Outline each Plasmodium falciparum-infected red blood cell.
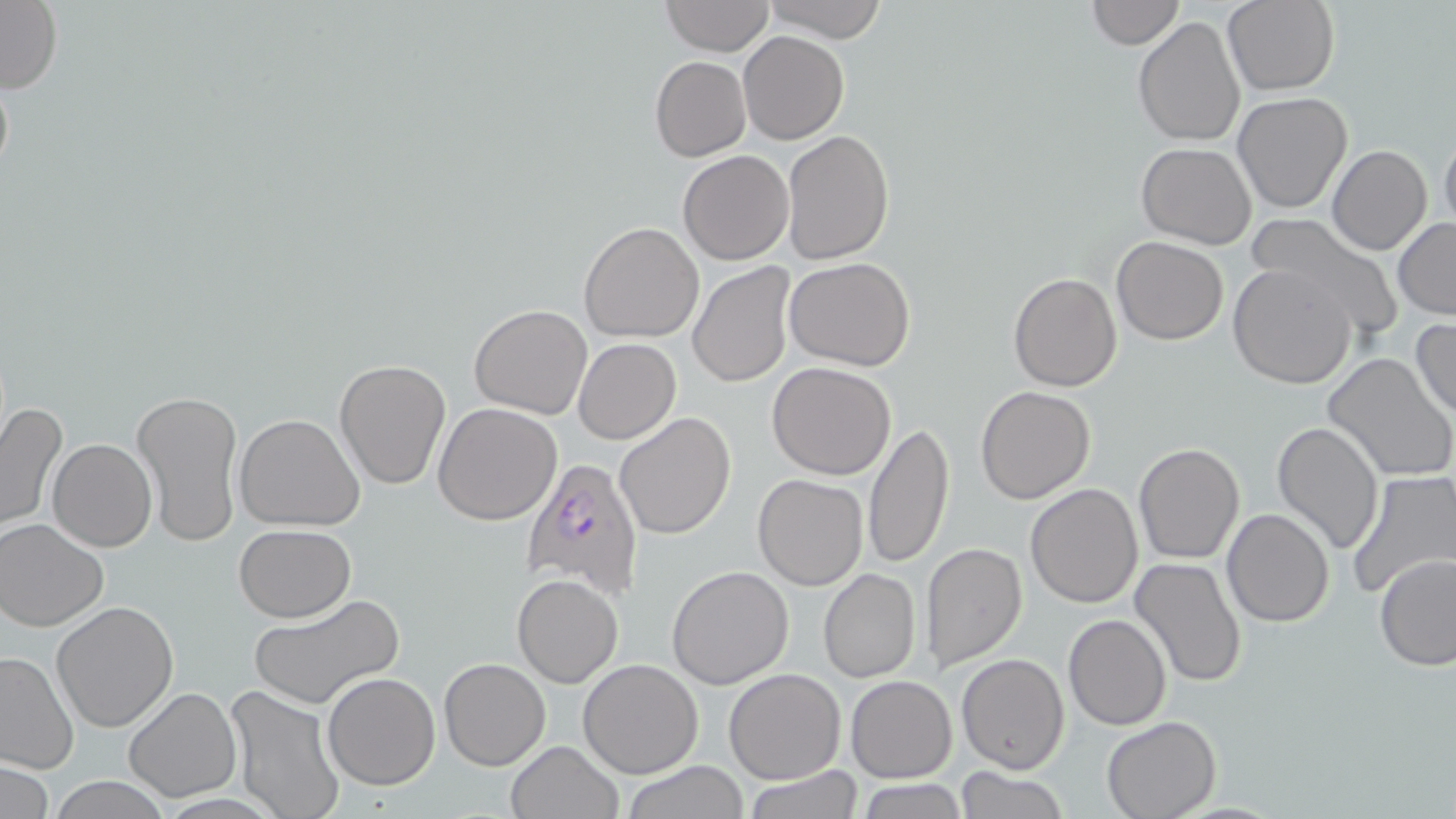

Approximate bounding boxes as (x1,y1)-(x2,y2) corner pairs in pixels.
Plasmodium falciparum-infected red blood cells: (520,457)-(645,599).

Uninfected red blood cell locations: (759,0)-(889,43), (660,1)-(775,56), (1084,1)-(1183,49), (1222,1)-(1341,96), (0,2)-(61,95), (1133,16)-(1247,148), (738,29)-(850,145), (650,55)-(751,161), (1232,93)-(1352,213), (1439,124)-(1456,231), (782,128)-(894,266), (1136,142)-(1257,248), (1327,144)-(1432,256), (678,149)-(794,264), (1242,213)-(1404,341), (1393,218)-(1456,320), (578,221)-(704,343), (1111,236)-(1229,346), (785,257)-(916,370), (688,262)-(795,388), (1228,264)-(1356,388), (1008,272)-(1123,391), (469,304)-(594,419), (1410,318)-(1456,420), (573,338)-(681,444), (1322,352)-(1455,483), (335,358)-(450,490), (766,362)-(898,480), (975,386)-(1095,503), (133,388)-(244,549), (1,399)-(69,534), (433,402)-(563,525), (614,411)-(737,540), (233,413)-(365,531), (863,420)-(954,570), (1269,420)-(1382,556), (47,439)-(157,552), (1132,443)-(1245,565), (1346,471)-(1456,601), (752,474)-(868,590), (1026,482)-(1143,607), (1222,508)-(1335,627), (0,519)-(109,632), (233,524)-(357,621), (918,542)-(1030,673), (1375,554)-(1456,670), (1128,556)-(1248,689), (666,565)-(794,690), (818,568)-(921,683), (512,574)-(623,686), (248,592)-(405,710), (50,602)-(179,733), (1062,612)-(1172,730), (0,652)-(77,774), (956,653)-(1069,772), (438,658)-(551,771), (577,658)-(704,778), (724,668)-(847,784), (321,673)-(441,791), (845,675)-(958,783), (223,684)-(347,819), (122,687)-(241,802), (1100,716)-(1220,819), (506,740)-(623,819), (2,760)-(53,819), (619,761)-(751,818), (952,765)-(1070,819), (746,766)-(865,819), (46,777)-(175,817), (858,779)-(968,818). Slide-level diagnosis: Plasmodium falciparum. Captured at 1000x magnification. May-Grünwald-Giemsa-stained preparation. Light microscopy. Thin blood film. Image is 1456×819 pixels. One field of a larger specimen.